Name the parasite shown.
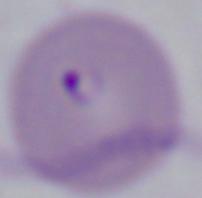

Babesia.

{
  "magnification": "1000x",
  "modality": "micrograph"
}